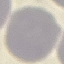

Summary:
  - Malaria status: uninfected
  - Capture: smartphone camera at the microscope eyepiece
  - Stain: Giemsa
  - Image type: automatically extracted cell patch, resized to 64 × 64 pixels
  - Preparation: thin blood smear